Identify the parasite.
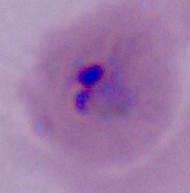
Plasmodium.

magnification = 400x or 1000x
modality = photomicrograph